Outline each blood parasite and name the species.
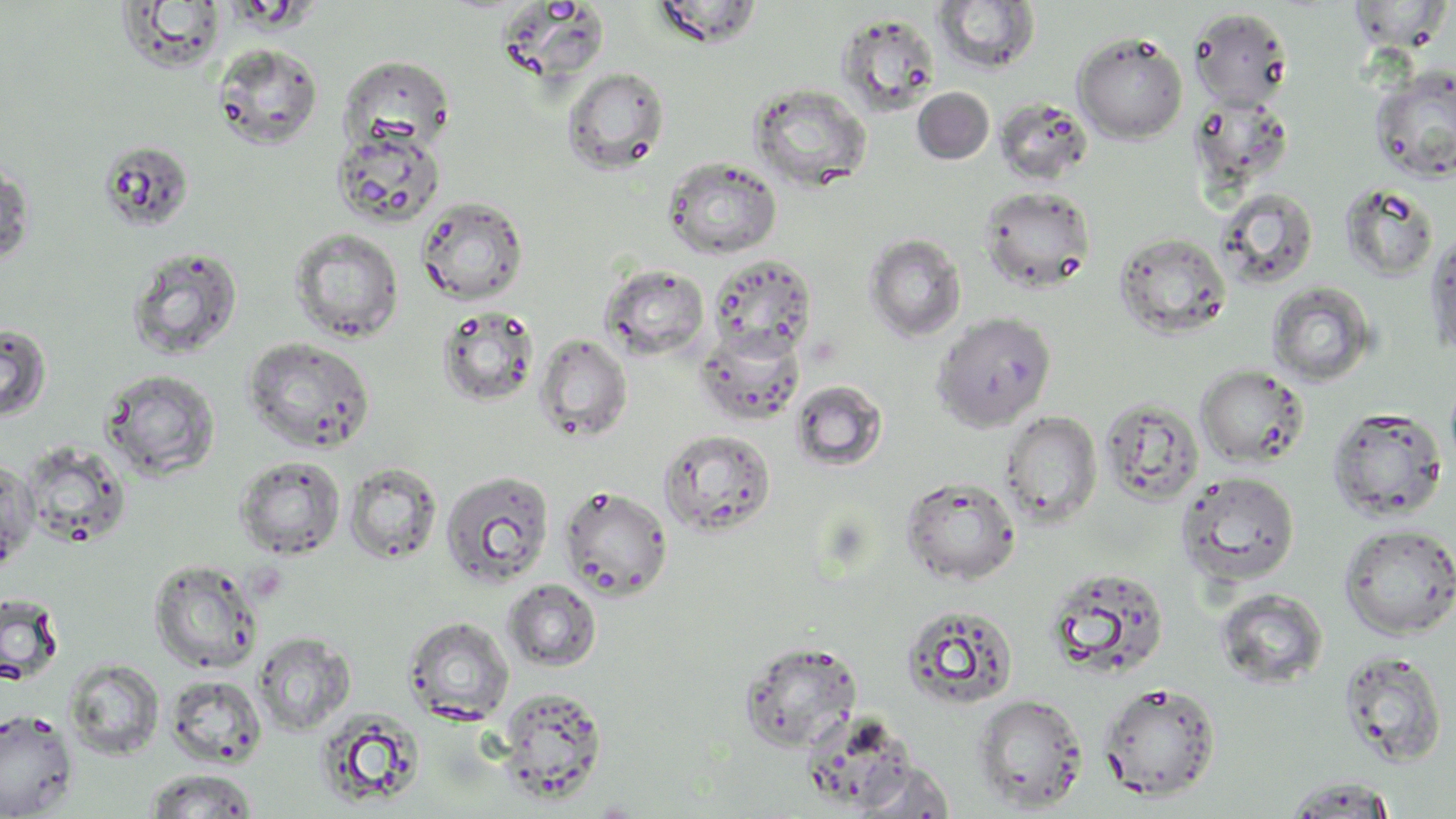
No blood parasites observed.

Summary:
  - Coordinate format: approximate bounding boxes as (x1, y1, x2, y2) in pixels
  - Uninfected red blood cell locations: (651, 0, 765, 48), (1347, 0, 1454, 54), (932, 1, 1041, 75), (114, 2, 229, 73), (1188, 7, 1293, 111), (836, 13, 941, 115), (1072, 32, 1188, 144), (211, 43, 324, 151), (338, 55, 455, 152), (1369, 65, 1456, 183), (562, 66, 670, 174), (748, 83, 873, 192), (912, 87, 995, 164), (994, 97, 1093, 185), (331, 127, 446, 229), (97, 140, 195, 233), (1, 155, 35, 268), (663, 156, 782, 260), (1341, 182, 1440, 282), (978, 186, 1097, 293), (1215, 187, 1319, 290), (416, 196, 529, 306), (1423, 224, 1456, 360), (289, 227, 404, 343), (1113, 231, 1232, 340), (864, 233, 967, 342), (125, 246, 244, 362), (707, 253, 818, 357), (601, 264, 710, 361), (1266, 282, 1379, 387), (436, 306, 540, 407), (931, 312, 1056, 432), (0, 322, 53, 423), (696, 327, 806, 426), (534, 333, 633, 443), (242, 337, 376, 453), (1195, 365, 1309, 467), (100, 368, 221, 480), (791, 380, 888, 472), (1099, 396, 1204, 508), (1327, 406, 1448, 523), (1000, 411, 1103, 527), (659, 428, 776, 537), (20, 441, 132, 549), (0, 448, 75, 561), (234, 455, 346, 560), (0, 456, 39, 574), (344, 462, 443, 565), (440, 470, 555, 590), (1176, 471, 1301, 587), (900, 476, 1021, 585), (559, 485, 673, 600), (1338, 523, 1456, 640), (148, 557, 264, 674), (1043, 565, 1171, 681), (504, 579, 602, 672), (1214, 587, 1328, 690), (0, 592, 64, 685), (901, 604, 1019, 710), (403, 616, 515, 725), (253, 632, 355, 735), (738, 641, 863, 752), (1337, 651, 1449, 769), (65, 658, 166, 760), (165, 675, 267, 768), (1097, 681, 1222, 802), (495, 686, 608, 802), (973, 694, 1088, 812), (0, 708, 79, 817), (314, 710, 426, 808), (845, 761, 957, 817), (144, 768, 259, 817), (1282, 777, 1402, 816)
  - Slide-level diagnosis: negative for blood parasites
  - Magnification: 1000x
  - Modality: optical microscopy
  - Field of view: one of a larger specimen
  - Image size: 1456×819 pixels
  - Preparation: thin blood smear
  - Stain: May-Grünwald-Giemsa